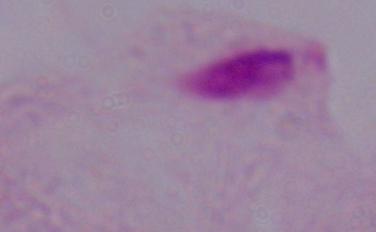 A trichomonad is shown. Photomicrograph. Captured at 1000x magnification.